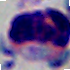
Summary:
  - Magnification: 1000x
  - Modality: micrograph
  - Identification: white blood cell